Mark where platelets are.
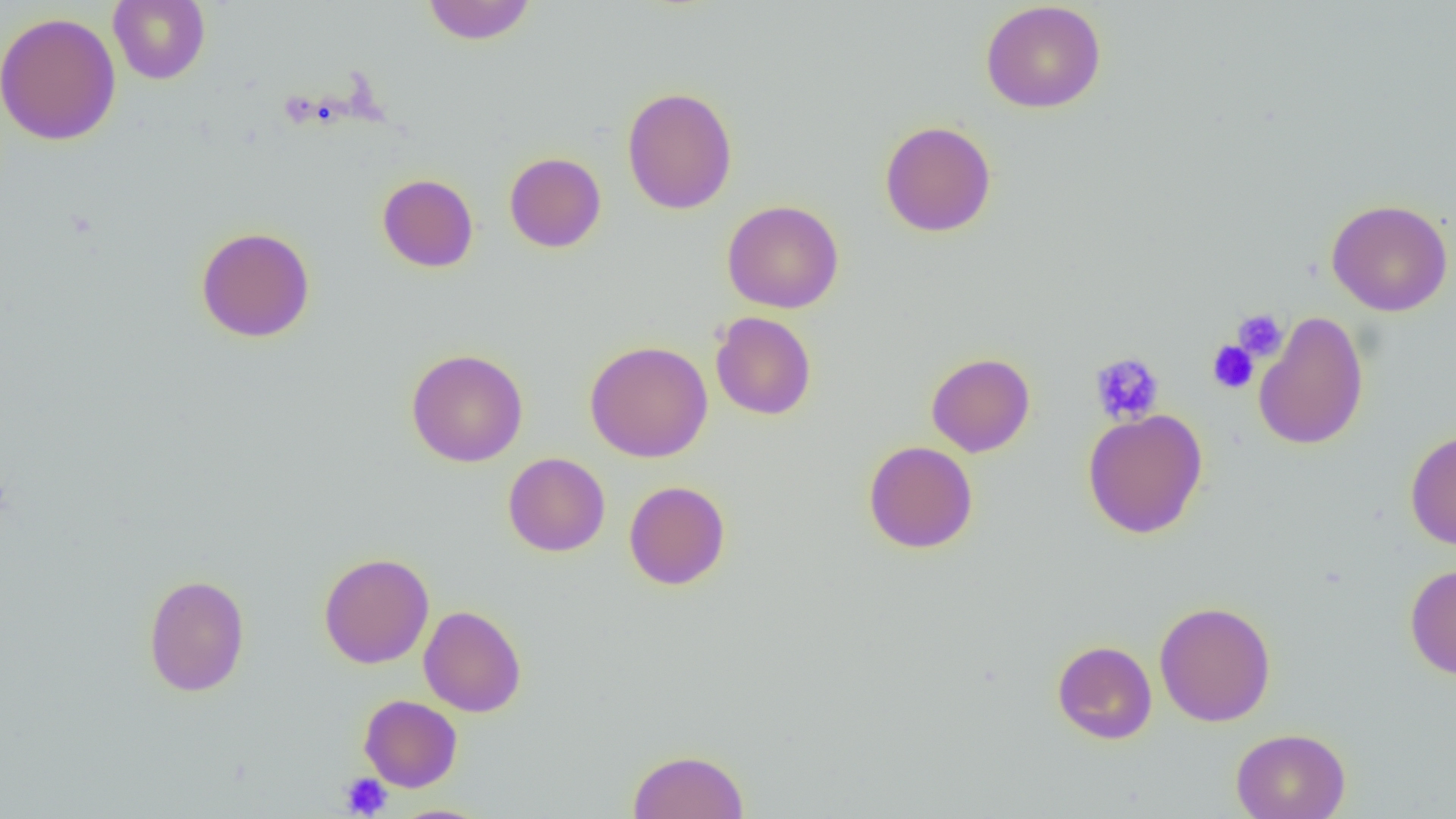

Approximate bounding boxes as [x1, y1, x2, y2] in pixels.
Platelets: [1231, 308, 1287, 362], [1207, 341, 1258, 393], [1089, 352, 1165, 426], [340, 773, 392, 817].

{
  "slide_level_diagnosis": "negative for blood parasites",
  "preparation": "thin blood smear",
  "modality": "optical microscopy",
  "field_of_view": "single",
  "uninfected_red_blood_cell_locations": "approximate bounding boxes as [x1, y1, x2, y2] in pixels: [108, 0, 210, 85], [422, 1, 537, 45], [980, 1, 1107, 114], [1, 11, 121, 146], [622, 86, 737, 215], [879, 120, 997, 237], [504, 152, 606, 253], [377, 173, 479, 272], [1326, 198, 1453, 317], [722, 199, 844, 314], [196, 226, 315, 343], [1252, 310, 1369, 450], [711, 311, 816, 420], [585, 340, 713, 462], [406, 349, 528, 467], [926, 352, 1035, 457], [1083, 408, 1208, 539], [1405, 428, 1456, 550], [863, 440, 978, 554], [503, 452, 610, 557], [624, 480, 730, 590], [318, 552, 434, 669], [1404, 562, 1456, 679], [143, 574, 250, 697], [1154, 600, 1276, 727], [419, 605, 527, 717], [1052, 640, 1157, 744], [359, 694, 463, 792], [1231, 728, 1350, 819], [627, 749, 749, 818], [386, 804, 495, 819]",
  "magnification": "1000x",
  "image_size": "1456×819 pixels"
}